Point out each Plasmodium parasite.
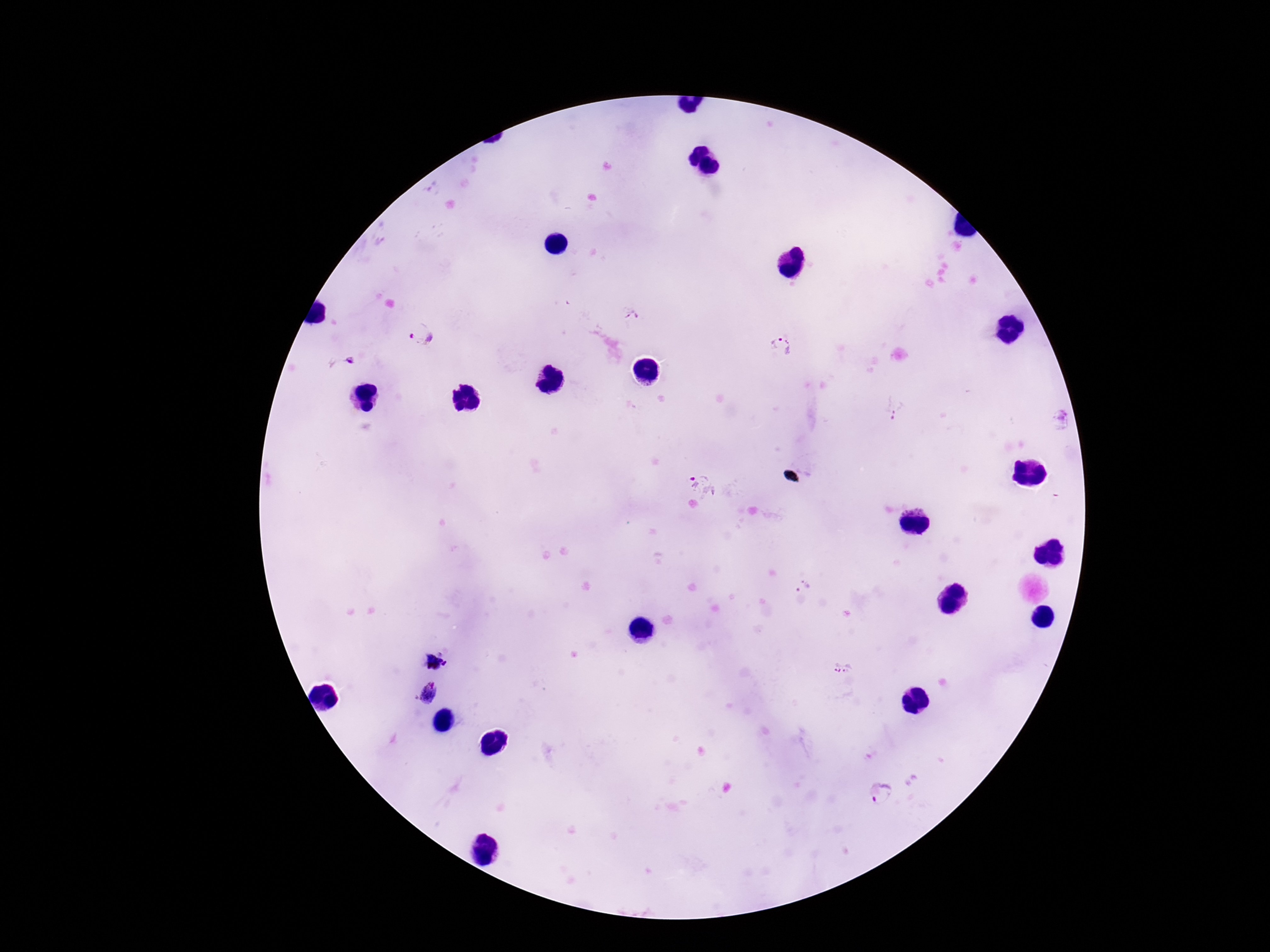
Approximate object centers, in pixels from the top-left corner.
Plasmodium parasites: (x=631, y=316), (x=423, y=336), (x=781, y=346), (x=349, y=360), (x=896, y=410), (x=1060, y=421), (x=705, y=485), (x=802, y=588), (x=841, y=667), (x=427, y=692), (x=885, y=794).

capture = smartphone camera through the microscope eyepiece
field of view = one from this slide
stain = Giemsa
image size = 1270×952 pixels
preparation = thick blood film
patient malaria status = positive
magnification = 100x